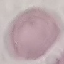
Summary:
  - Result: negative for malaria parasites
  - Image type: automatically extracted cell patch, resized to 64 × 64 pixels
  - Preparation: thin blood film
  - Stain: Giemsa
  - Capture: smartphone through the microscope eyepiece